Comment on the morphology of the erythrocytes.
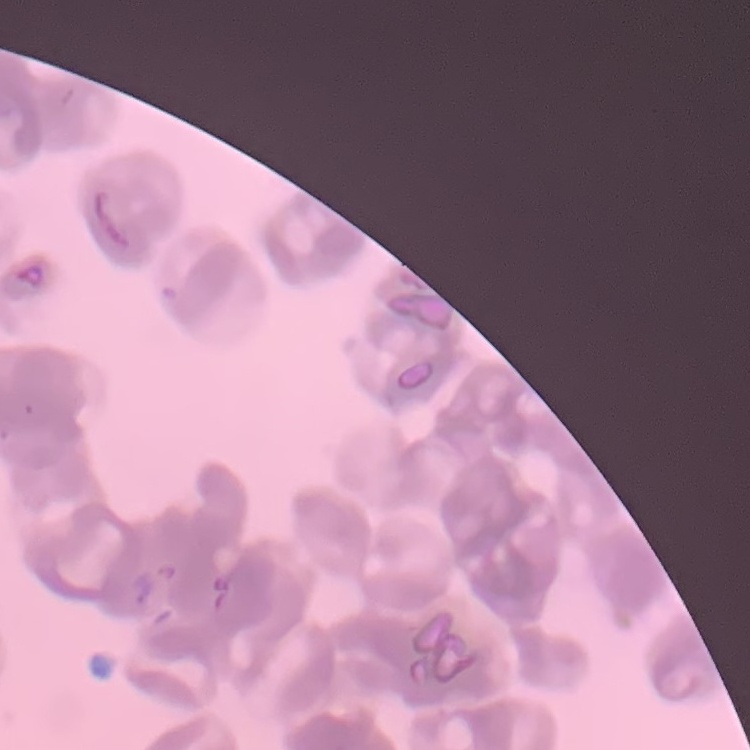

They show rouleaux formation.

{
  "image_type": "one tile cut from a larger photomicrograph",
  "preparation": "thin blood smear",
  "stain": "Field's or Giemsa"
}